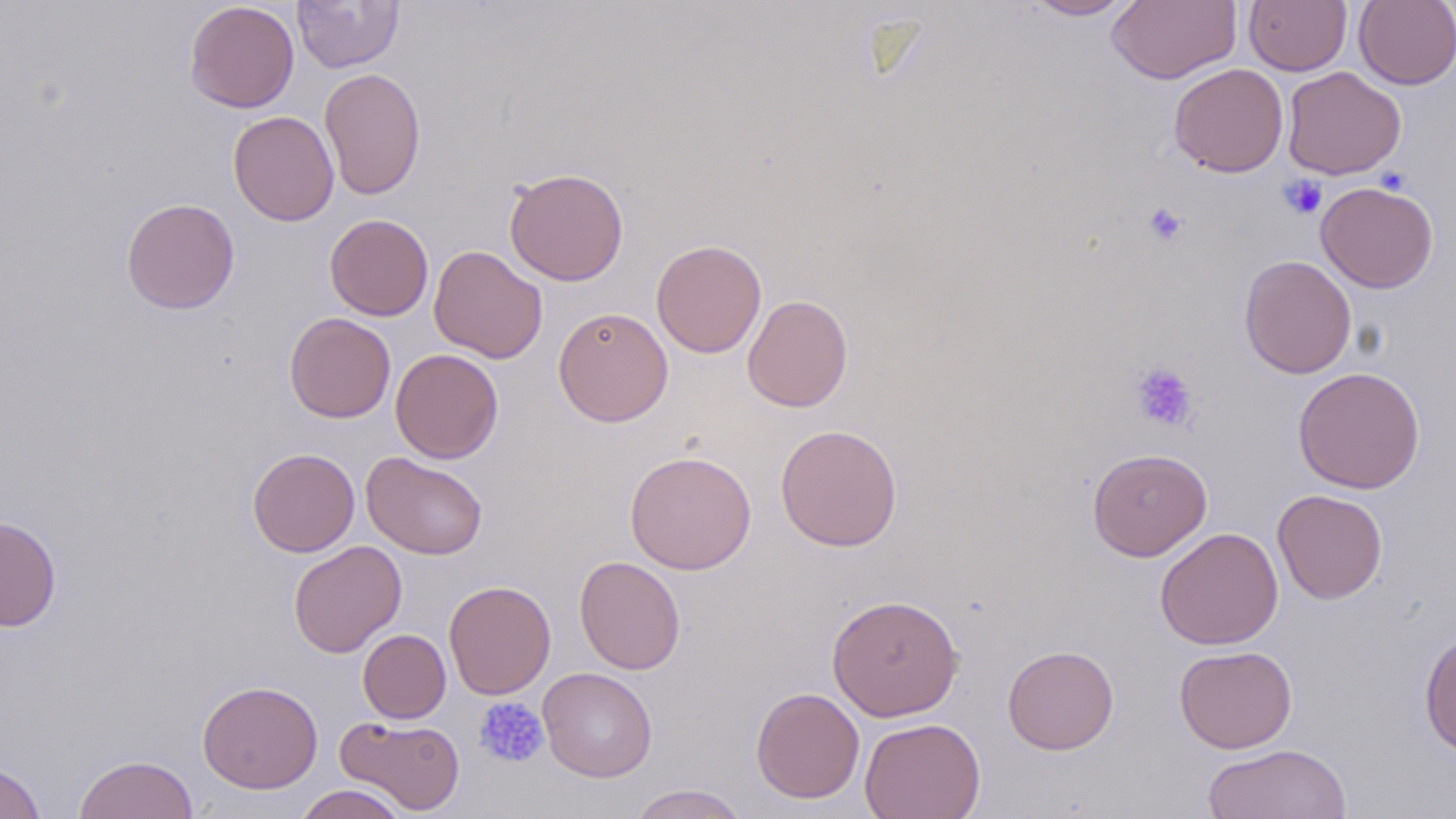

Approximate bounding boxes as (x1, y1, x2, y2) in pixels. Platelet locations: (1279, 175, 1327, 220), (1143, 202, 1188, 247), (1129, 362, 1199, 433), (473, 696, 549, 768). Uninfected red blood cell locations: (292, 0, 404, 73), (1021, 0, 1139, 20), (1106, 0, 1241, 84), (1244, 0, 1352, 76), (1353, 0, 1456, 90), (184, 1, 299, 113), (1169, 63, 1288, 177), (319, 67, 425, 201), (1282, 67, 1405, 180), (228, 110, 339, 226), (504, 167, 629, 286), (1315, 181, 1439, 293), (121, 197, 240, 314), (325, 214, 433, 321), (651, 240, 767, 358), (429, 245, 547, 363), (1240, 255, 1357, 379), (742, 295, 853, 412), (553, 306, 673, 427), (284, 312, 396, 423), (390, 348, 503, 463), (1293, 366, 1425, 493), (775, 424, 902, 551), (247, 448, 360, 557), (1087, 448, 1212, 561), (625, 449, 756, 575), (361, 451, 488, 560), (1272, 488, 1388, 604), (0, 515, 61, 632), (1155, 527, 1283, 650), (287, 540, 407, 658), (574, 555, 686, 675), (444, 580, 556, 699), (827, 593, 963, 721), (1419, 628, 1456, 758), (358, 629, 451, 723), (1002, 644, 1119, 754), (1175, 645, 1297, 753), (538, 667, 658, 782), (197, 680, 323, 794), (751, 687, 865, 804), (334, 715, 466, 815), (860, 717, 985, 819), (1203, 743, 1351, 819), (73, 754, 199, 818), (0, 762, 46, 819), (294, 784, 408, 819), (628, 784, 750, 818). Slide-level diagnosis: no evidence of blood parasites. Thin blood film. Optical microscopy. Single field of view. May-Grünwald-Giemsa-stained preparation. Captured at 1000x magnification. Image is 1456×819 pixels.